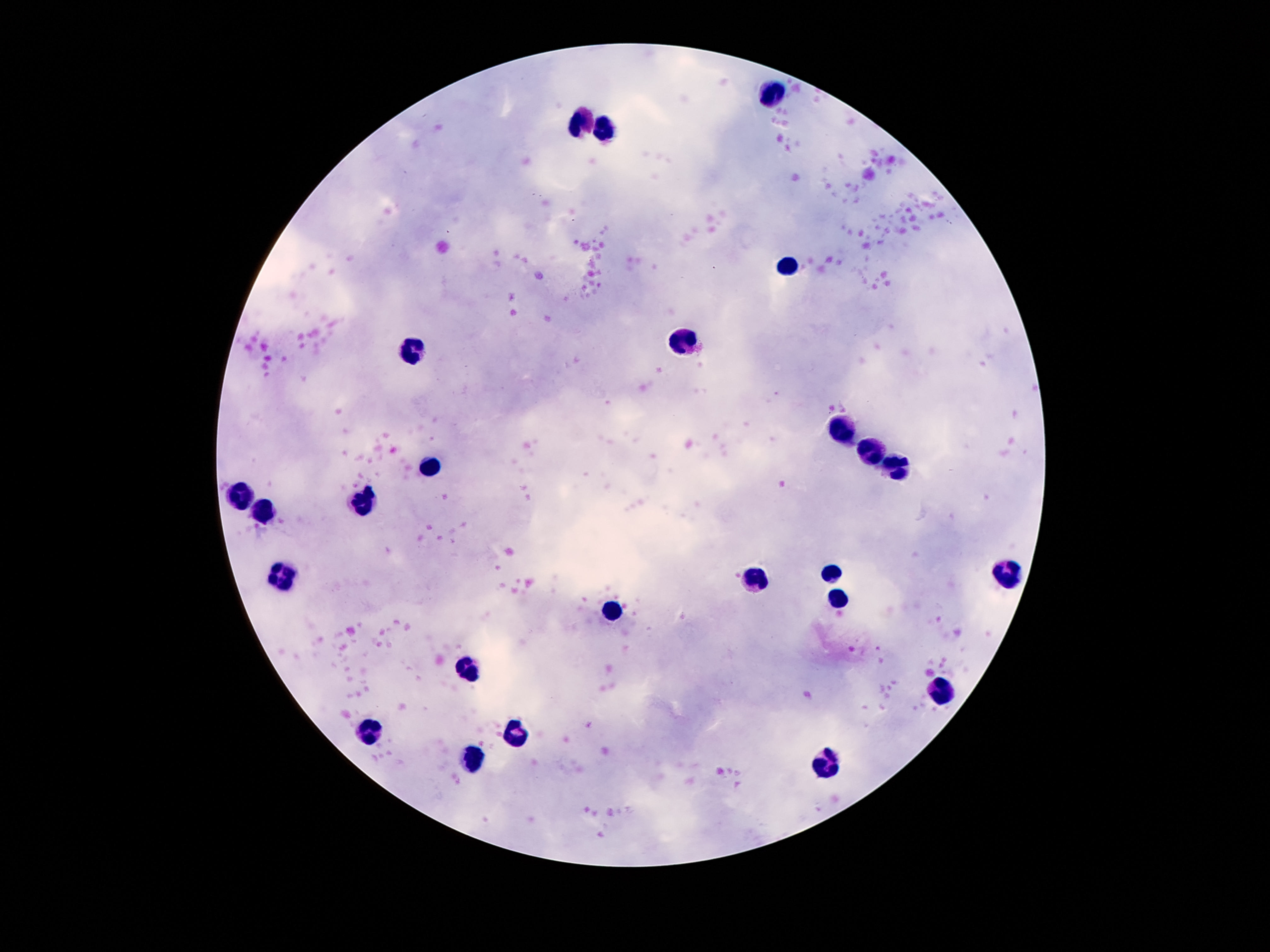

{
  "stain": "Giemsa",
  "leukocyte_locations": "approximate object centers, in pixels from the top-left corner: (x=770, y=92), (x=579, y=123), (x=608, y=132), (x=788, y=264), (x=680, y=343), (x=410, y=353), (x=839, y=430), (x=870, y=451), (x=430, y=465), (x=893, y=469), (x=240, y=500), (x=366, y=500), (x=268, y=512), (x=831, y=571), (x=1005, y=572), (x=280, y=573), (x=755, y=579), (x=837, y=602), (x=612, y=610), (x=469, y=667), (x=940, y=692), (x=371, y=735), (x=514, y=735), (x=473, y=760), (x=827, y=765)",
  "magnification": "100x",
  "preparation": "thick blood film",
  "image_size": "1270×952 pixels",
  "field_of_view": "single",
  "capture": "smartphone camera through the microscope eyepiece",
  "patient_malaria_status": "negative"
}